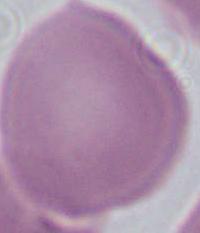 An erythrocyte is shown. Micrograph. Captured at 1000x magnification.